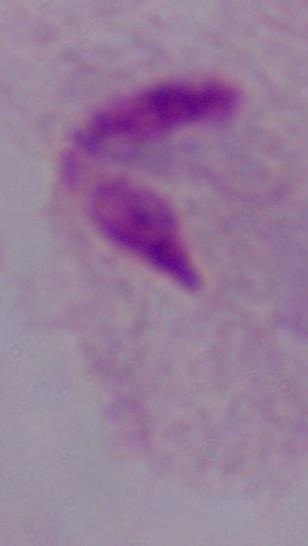

Summary:
  - Magnification: 1000x
  - Identification: trichomonad
  - Modality: micrograph